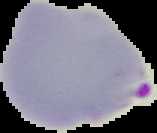
Malaria status: parasitized. Image is 157×133 pixels. From a thin blood film. Segmented cell region on a black background.